Identify the cell.
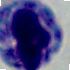

This is a leukocyte.

Captured at 1000x magnification. Micrograph.